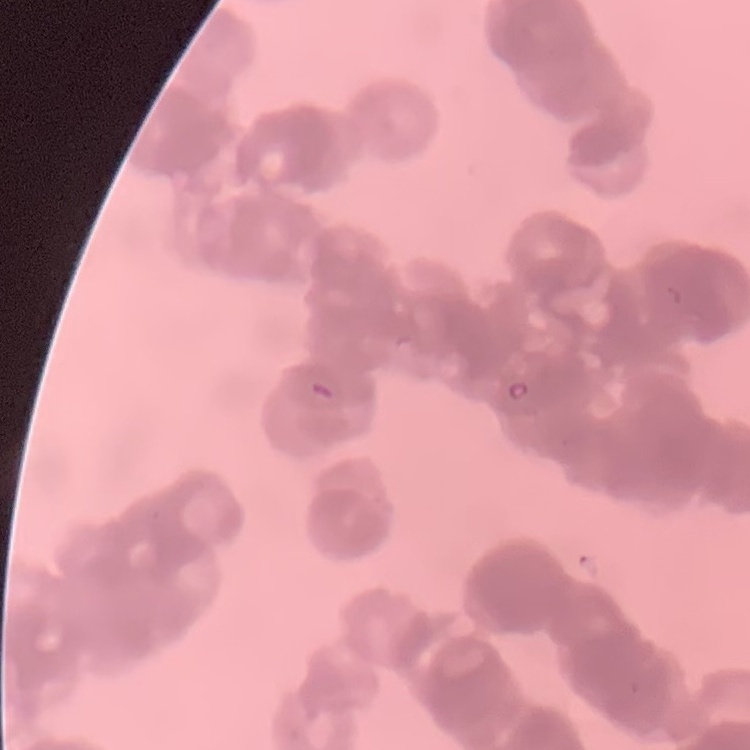 The erythrocytes show rouleaux formation. One tile cut from a larger photomicrograph. Thin peripheral smear. Field's or Giemsa stain.